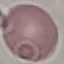

Summary:
  - Malaria status: uninfected
  - Preparation: thin blood smear
  - Stain: Giemsa
  - Image type: cell patch, automatically extracted from a larger field of view and resized to 64 × 64 pixels
  - Capture: smartphone camera at the microscope eyepiece